Identify the preparation type.
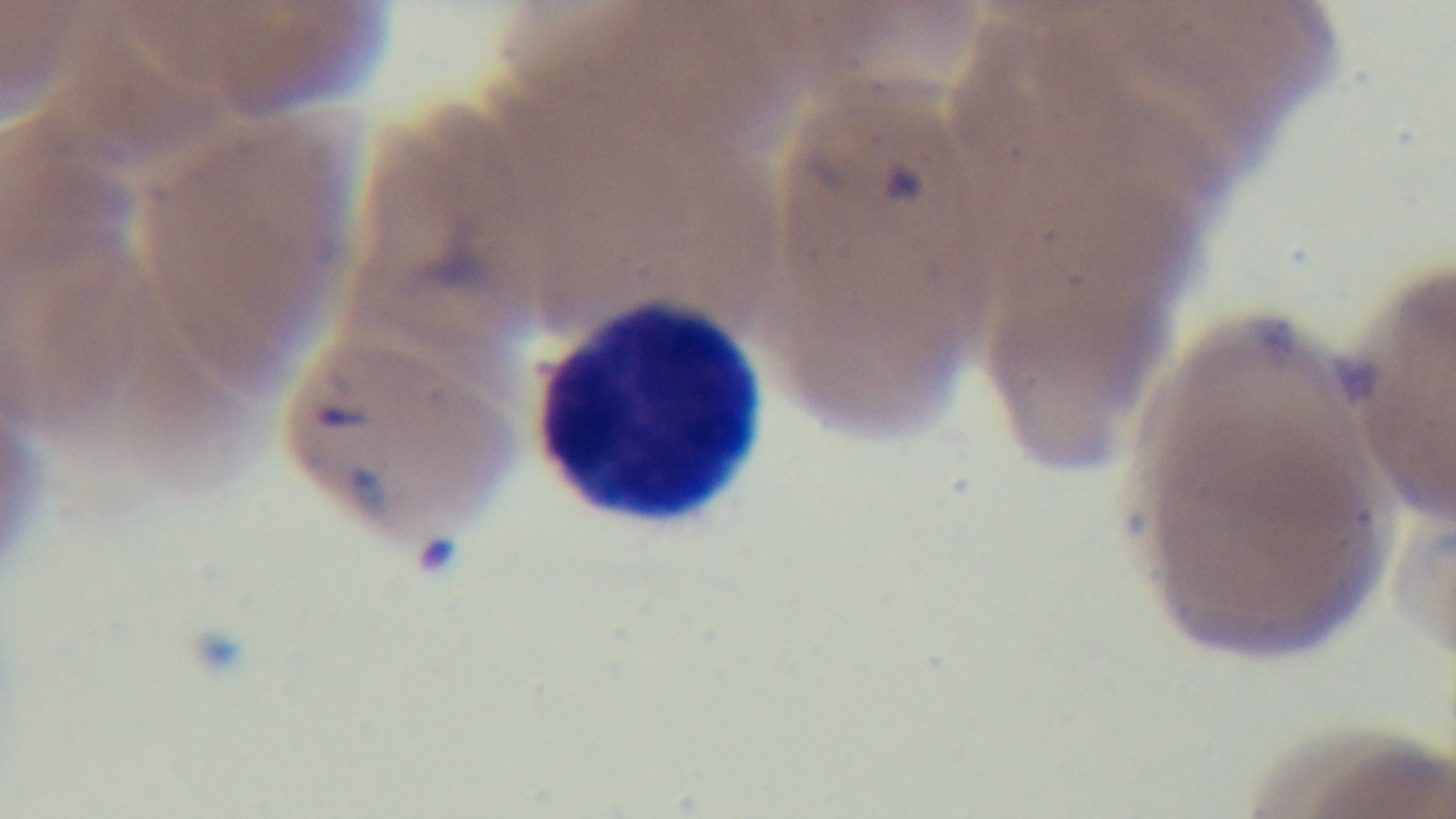

It is a thin blood film.

capture = mounted 4K digital camera
modality = light microscopy
malaria status = infected
stain = Giemsa
objective = 100x oil immersion
field of view = single